Assess for Plasmodium parasites.
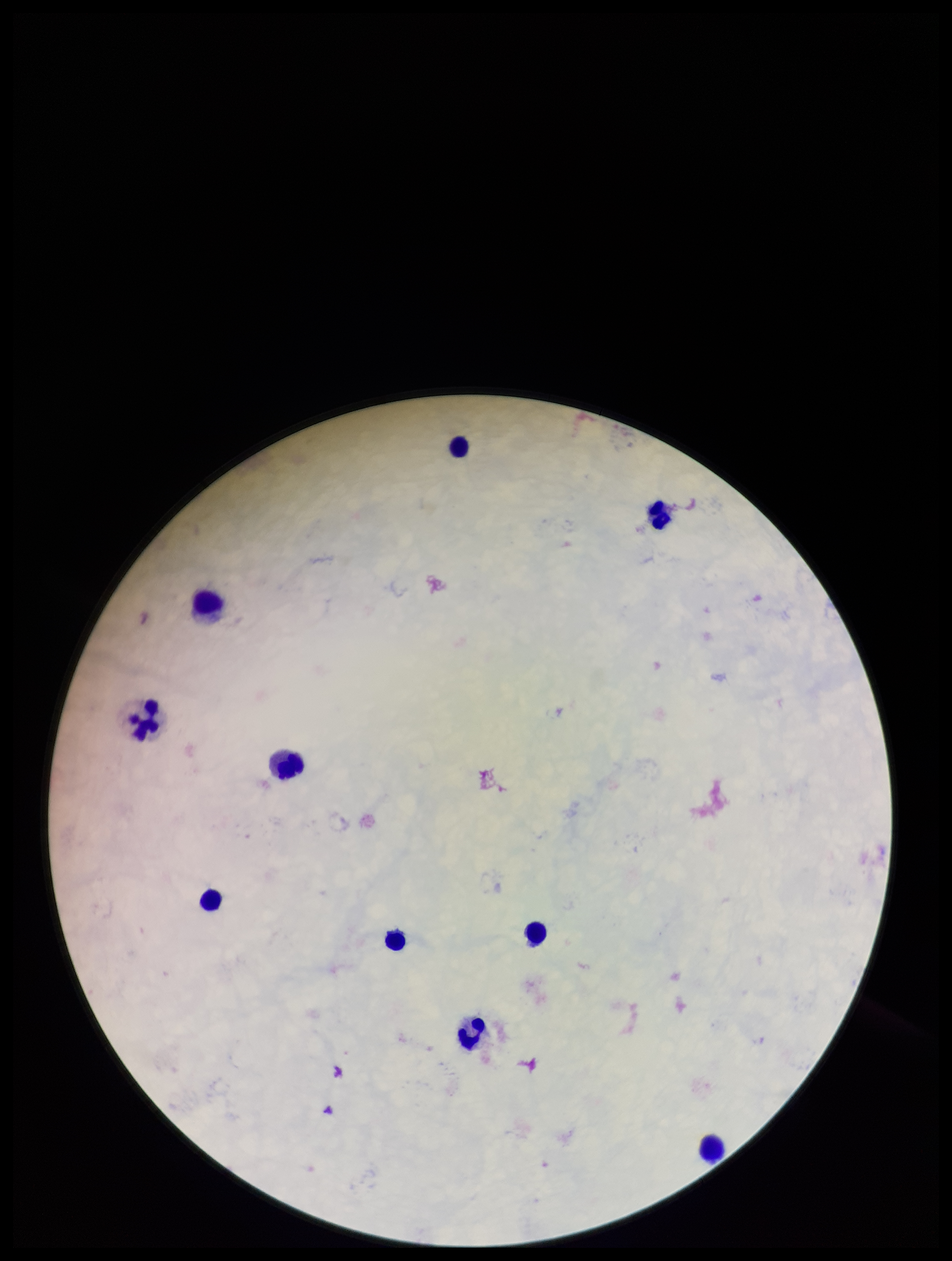

None detected.

Preparation: thick blood smear. Leukocyte count: 10. Patient malaria status: negative. Photographed through the microscope eyepiece with a smartphone camera. Image is 952×1261 pixels. Stained with Giemsa. Parasite count: 0. Single field of view.